Assess this cell for malaria.
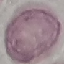

It is uninfected.

Automatically extracted cell patch, resized to 64 × 64 pixels. Photographed with a smartphone camera at the microscope eyepiece. Giemsa stain. Thin blood smear.